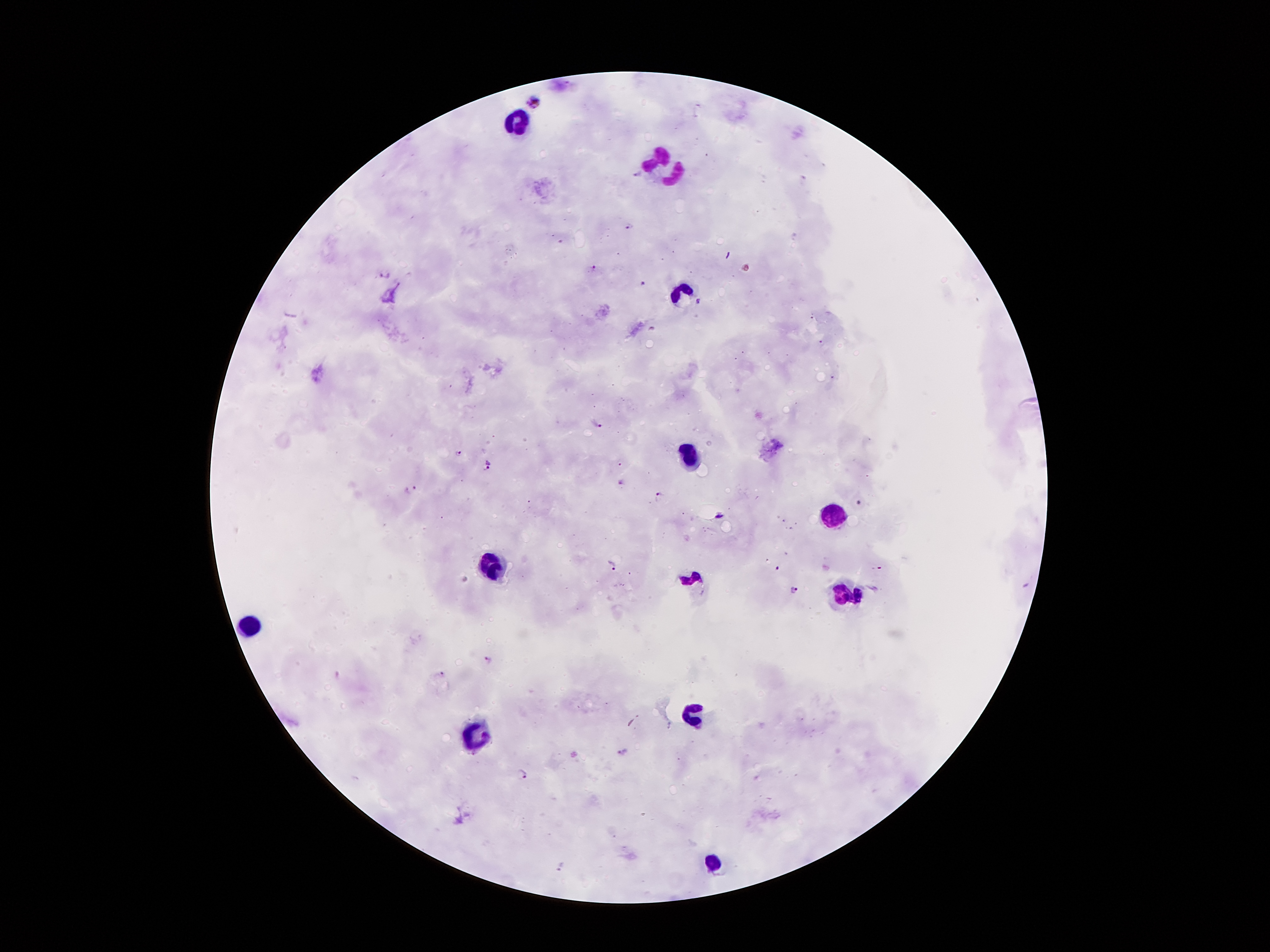
Approximate centers as [x, y] in pixels. Plasmodium parasite locations: [532, 98], [639, 173], [628, 226], [595, 268], [386, 274], [642, 284], [700, 301], [813, 318], [652, 329], [821, 342], [833, 376], [599, 424], [459, 453], [621, 464], [488, 466], [623, 482], [412, 488], [658, 496], [611, 565], [777, 567], [876, 569], [795, 590], [488, 660], [440, 672], [521, 775], [562, 868]. Leukocyte locations: [519, 123], [670, 171], [685, 288], [692, 454], [835, 514], [494, 565], [690, 579], [846, 596], [251, 623], [689, 710], [478, 739], [712, 862]. One field from this slide. Giemsa-stained preparation. Image is 1270×952 pixels. 100x magnification. Smartphone photograph taken through the microscope eyepiece. Patient malaria status: infected with Plasmodium falciparum. Thick peripheral-blood smear.